Classify this cell by malaria status.
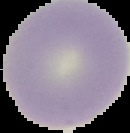

It is uninfected.

The area outside the segmented cell region is set to black. From a thin blood film. Image is 130×133 pixels.